Name the blood parasite species.
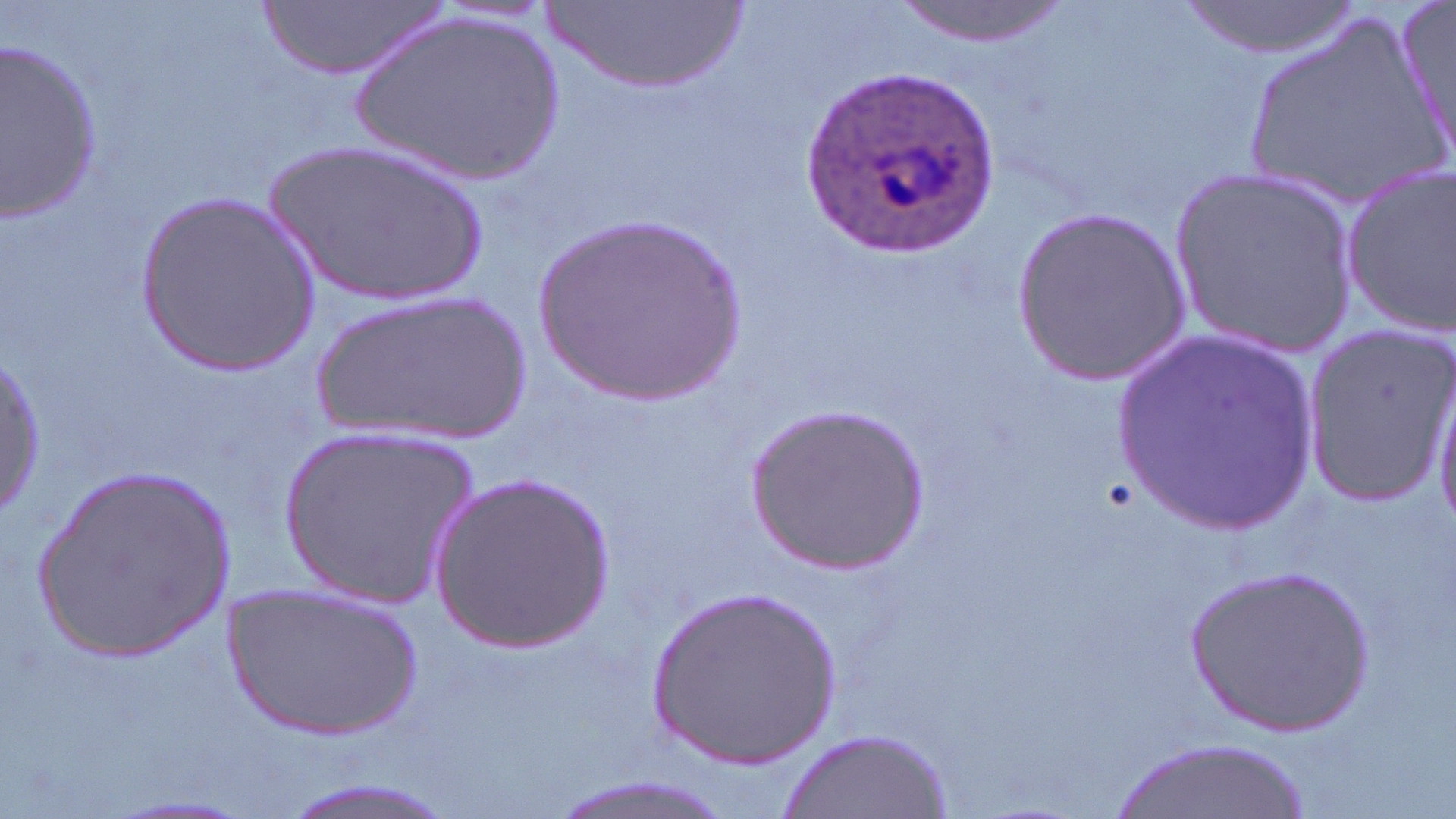
Plasmodium ovale.

Approximate bounding boxes as (x1,y1)-(x2,y2) corner pairs in pixels. Plasmodium ovale-infected red blood cell locations: (804,69)-(995,256). Uninfected red blood cell locations: (263,0)-(447,82), (545,0)-(743,92), (893,0)-(1072,46), (1176,0)-(1363,62), (1397,5)-(1456,167), (1232,9)-(1446,209), (352,11)-(568,185), (0,33)-(104,223), (267,136)-(495,308), (1340,162)-(1455,339), (1171,165)-(1359,355), (138,190)-(320,375), (1013,203)-(1192,382), (528,215)-(750,409), (310,291)-(533,442), (1300,325)-(1456,507), (1113,332)-(1324,534), (2,352)-(45,520), (1427,375)-(1456,534), (740,400)-(929,576), (279,427)-(480,607), (30,466)-(239,664), (430,470)-(615,651), (1184,563)-(1373,738), (219,580)-(425,740), (646,587)-(842,773), (778,729)-(954,819), (1115,738)-(1304,819), (542,774)-(742,819), (274,777)-(456,819), (106,795)-(254,817). Single field of view. 1000x magnification. Optical microscopy. Thin blood smear. May-Grünwald-Giemsa-stained preparation. Image is 1456×819 pixels.